Assess this cell for malaria.
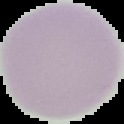

It is uninfected.

Summary:
  - Image type: segmented cell region with the area outside set to black
  - Image size: 124×124 pixels
  - Preparation: thin blood film